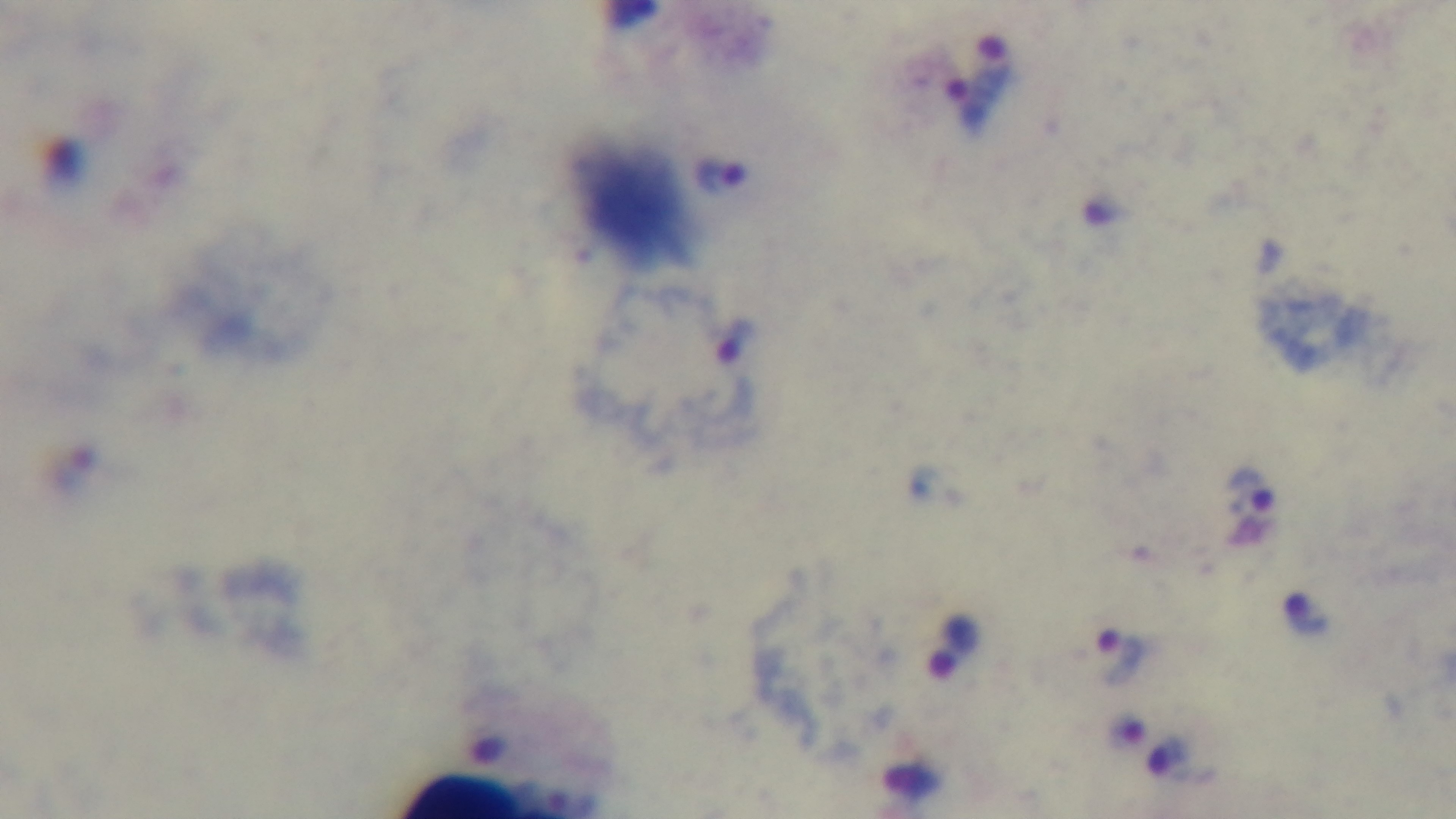 Preparation: thick smear. 100x oil-immersion objective. One field from the slide. Mounted 4K digital camera. Giemsa-stained. Photomicrograph. Malaria status: positive.